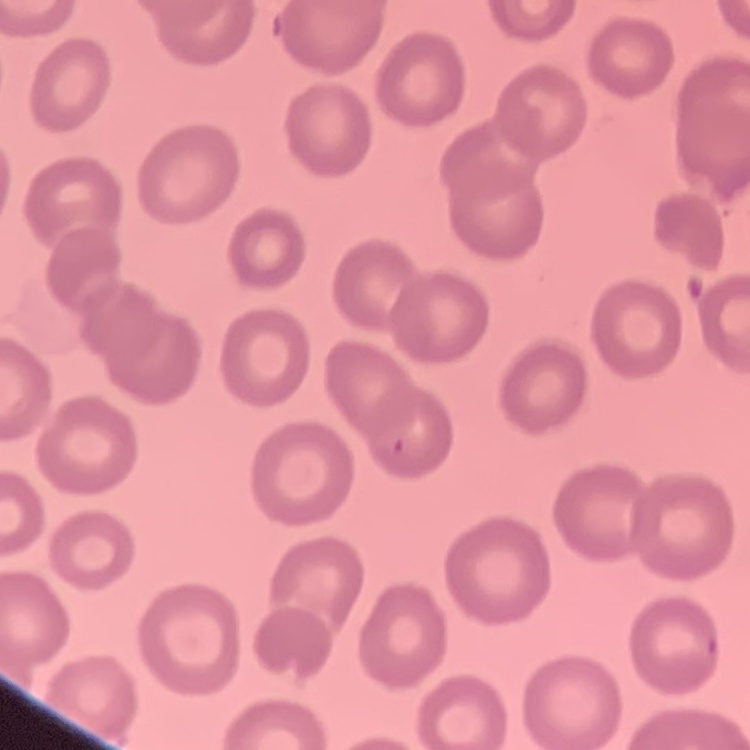
erythrocyte_morphology: no rouleaux formation
image_type: square crop of a larger photomicrograph
stain: Field's or Giemsa
preparation: thin blood film